Assess this cell for malaria.
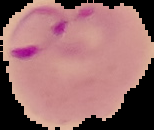
Parasitized.

Cell region segmented out of the field of view; the surrounding area is masked to black. Image is 154×130 pixels. From a thin blood smear.